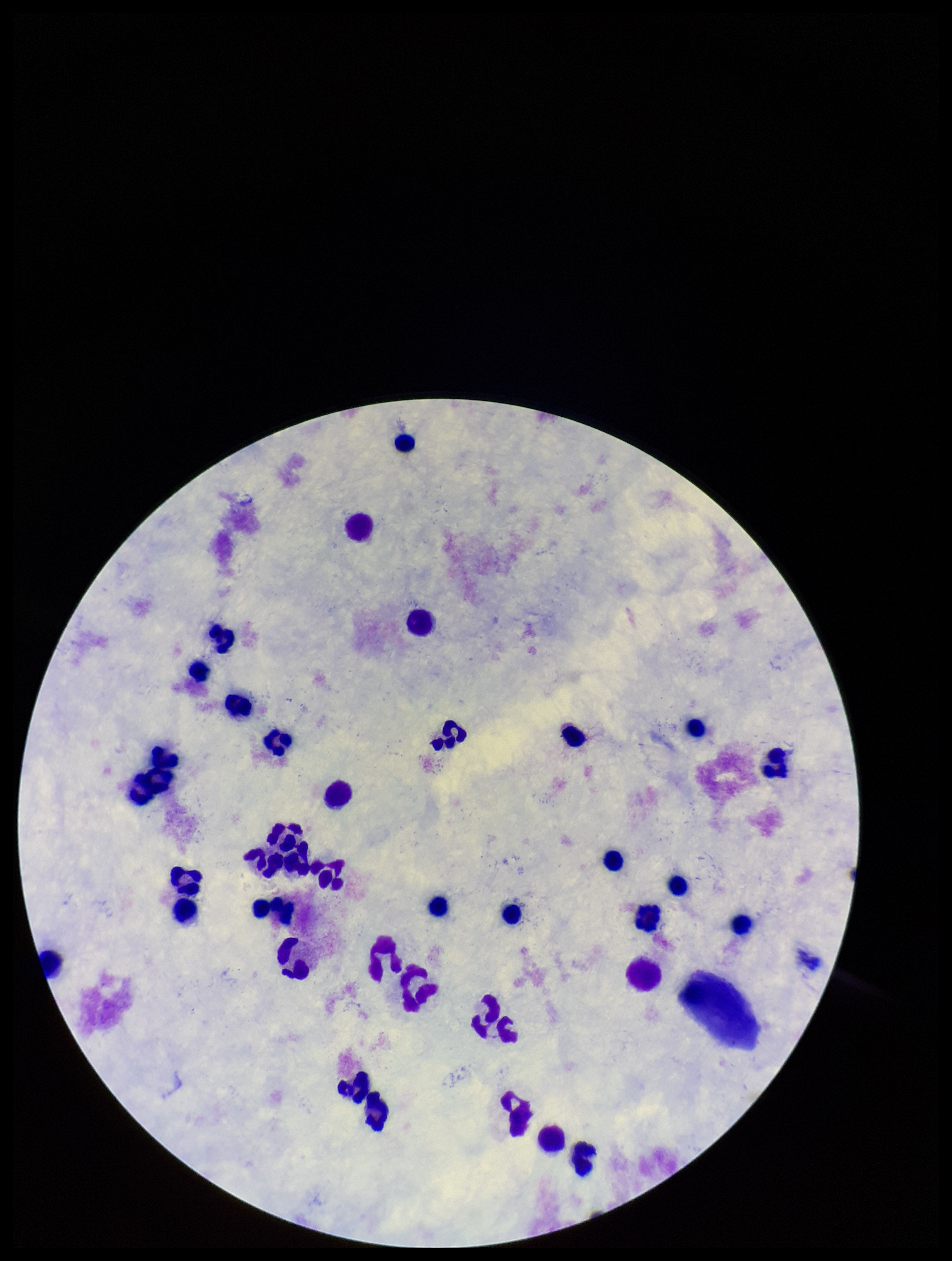

preparation = thick smear
capture = smartphone photograph through the microscope eyepiece
field of view = single
leukocyte count = 34
parasite count = 0
Plasmodium parasites = none detected
patient malaria status = negative
stain = Giemsa
image size = 952×1261 pixels